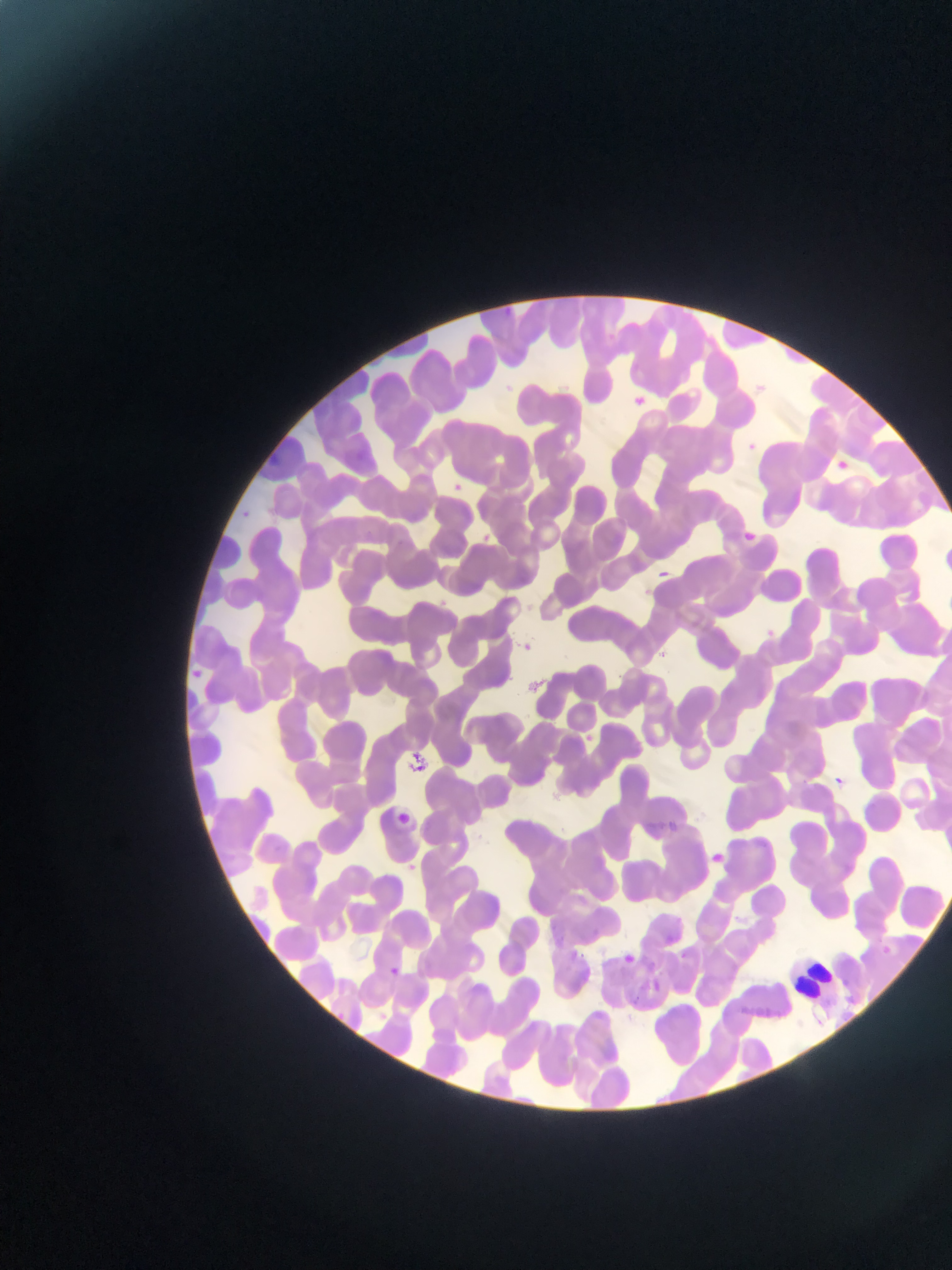 Approximate bounding boxes as left top right bottom in pixels. Leukocyte locations: 798 949 838 1007. Artifact (stain precipitate or debris) locations: 411 748 432 772. Malaria parasite locations: 626 392 651 414; 829 454 855 478; 447 479 466 497; 244 508 258 520; 741 526 758 543; 476 531 494 548; 661 569 667 579; 762 626 778 641; 518 639 537 655; 186 665 206 683; 576 733 596 750; 827 773 849 794; 388 810 414 830; 671 820 681 834; 703 847 728 870; 401 859 420 876; 620 947 641 966; 385 964 404 983; 652 977 665 992; 329 1008 349 1025. Thin blood smear. Photographed through a microscope with a mobile-phone camera. One field of view. Collected in Ghana. Image is 952×1270 pixels.